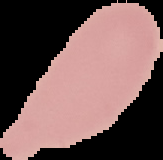

image type = cell region segmented out of the field of view; surrounding area masked to black
preparation = thin blood film
image size = 163×160 pixels
result = no malaria parasites seen